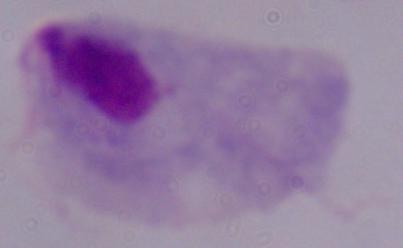
A trichomonad is seen. Captured at 1000x magnification. Micrograph.